Comment on the morphology of the red blood cells.
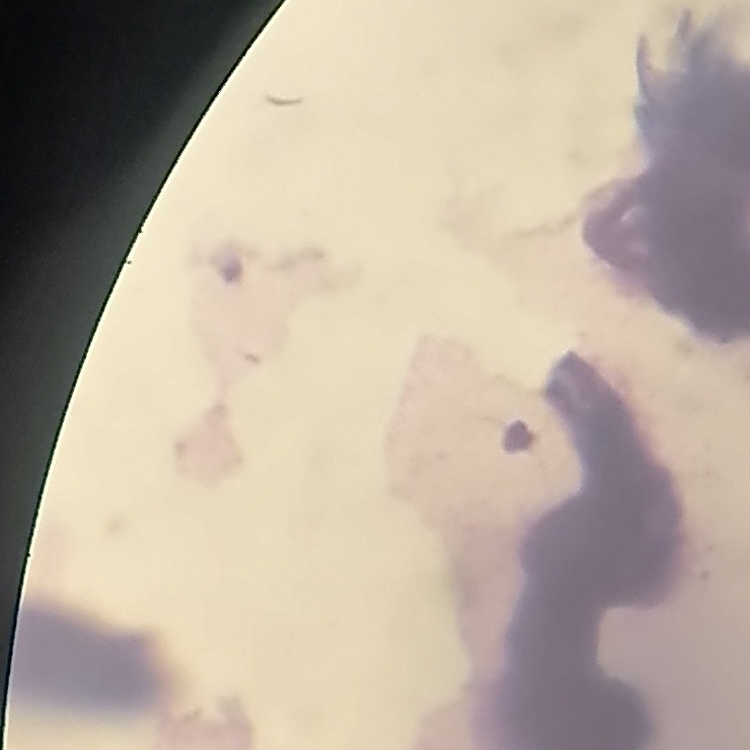

They show rouleaux formation.

Field's or Giemsa stain. Square crop of a larger photomicrograph. Thin blood smear.